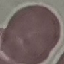

Result: no malaria parasites detected. Photographed with a smartphone camera at the microscope eyepiece. Giemsa stain. Thin blood film. Automatically extracted cell patch, resized to 64 × 64 pixels.